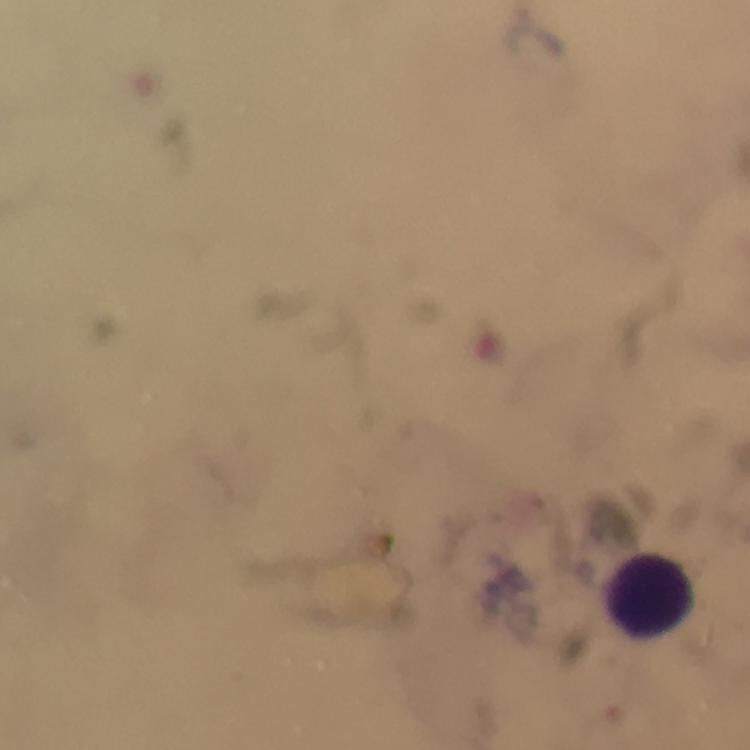
immersion_oil: applied
leukocyte_locations: 'approximate centers as [x, y] in pixels: [651, 591]'
magnification: 100x
image_size: 750×750 pixels
cropped_from: one field of view
capture: smartphone mounted on the microscope
preparation: thick smear
stain: Giemsa
context: from a diagnostic examination for malaria
plasmodium_parasites: none seen